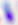

400x magnification. Toxoplasma gondii is seen. Photomicrograph.